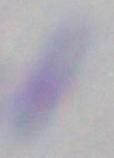
modality: photomicrograph
magnification: 1000x
identification: Toxoplasma gondii